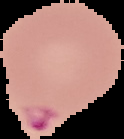
Image is 124×139 pixels. The area outside the segmented cell region is set to black. Malaria status: parasitized. From a thin blood film.